State the blood parasite species.
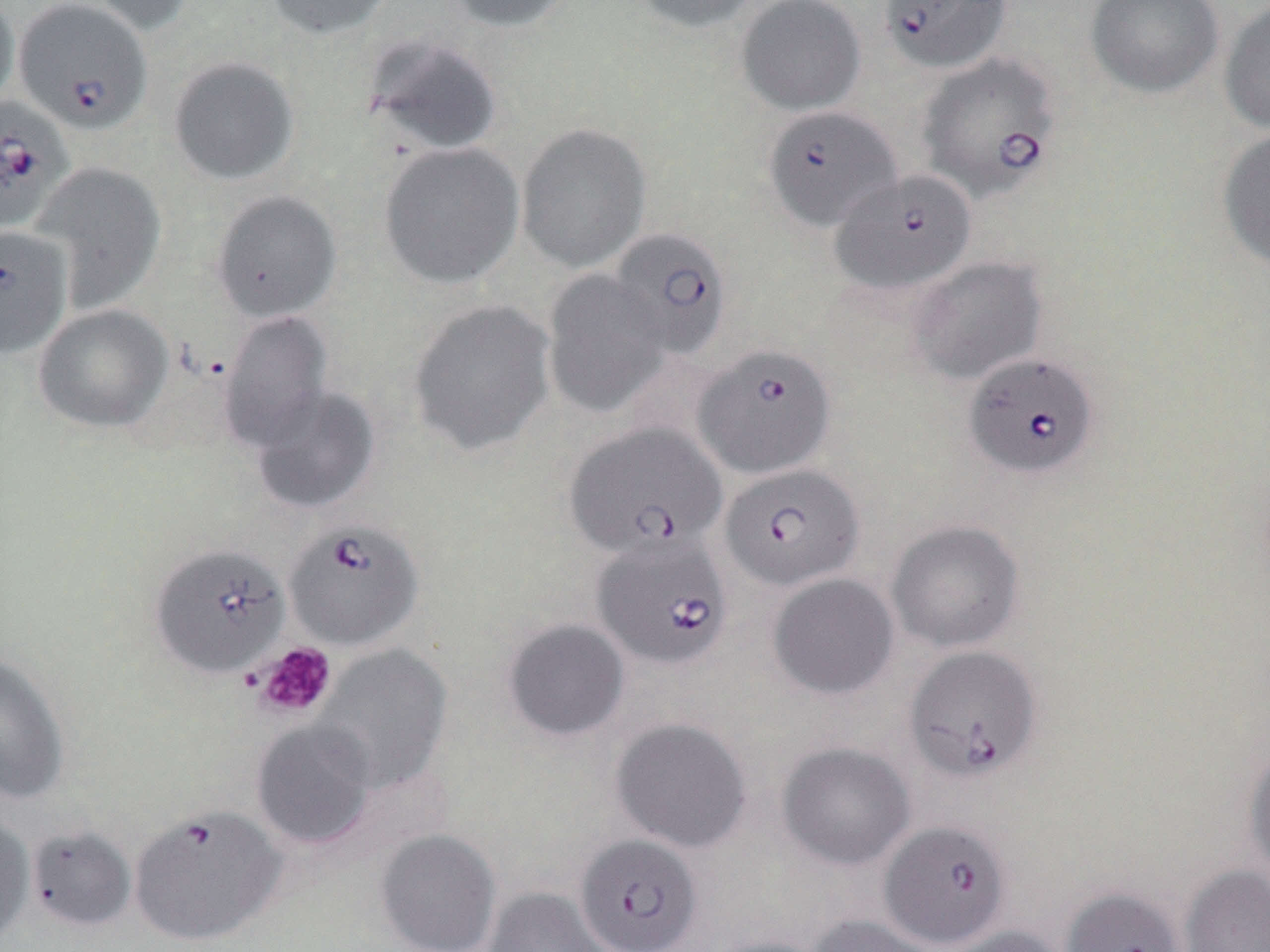

Babesia divergens.

stain = May-Grünwald-Giemsa
platelet locations = approximate bounding boxes as (x1,y1)-(x2,y2) corner pairs in pixels: (251,641)-(337,720)
magnification = 1000x
field of view = single
Babesia divergens-infected red blood cell locations = approximate bounding boxes as (x1,y1)-(x2,y2) corner pairs in pixels: (13,0)-(152,135), (878,0)-(1012,74), (916,52)-(1063,202), (0,95)-(71,233), (761,105)-(901,232), (830,169)-(977,295), (0,226)-(72,358), (606,227)-(733,359), (692,343)-(836,479), (964,352)-(1100,479), (564,424)-(728,563), (719,463)-(864,592), (283,519)-(424,651), (592,533)-(733,671), (149,544)-(290,679), (905,645)-(1042,783), (129,805)-(286,946), (880,820)-(1012,948), (574,833)-(703,952)
modality = optical microscopy
preparation = thin blood smear
image size = 1270×952 pixels
uninfected red blood cell locations = approximate bounding boxes as (x1,y1)-(x2,y2) corner pairs in pixels: (0,0)-(20,113), (76,0)-(198,36), (264,0)-(397,40), (445,0)-(579,33), (628,0)-(765,34), (1085,0)-(1225,99), (735,1)-(867,116), (1219,1)-(1270,134), (362,33)-(503,157), (168,55)-(300,186), (516,123)-(651,272), (1216,127)-(1270,273), (379,142)-(525,290), (34,162)-(166,311), (210,190)-(342,322), (907,256)-(1047,384), (541,270)-(672,419), (406,299)-(557,457), (33,304)-(173,434), (218,311)-(335,452), (250,385)-(381,514), (886,519)-(1025,653), (767,573)-(900,699), (501,618)-(630,742), (314,643)-(452,794), (0,652)-(70,804), (610,717)-(753,853), (251,718)-(379,850), (1242,740)-(1270,883), (776,741)-(916,871), (0,813)-(35,945), (26,824)-(137,933), (375,829)-(501,952), (1180,864)-(1270,952), (482,887)-(616,952), (1060,887)-(1185,952), (806,914)-(945,952), (939,925)-(1070,952), (702,935)-(834,952)